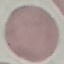

{
  "result": "no malaria parasites detected",
  "preparation": "thin blood smear",
  "capture": "smartphone camera at the microscope eyepiece",
  "image_type": "automatically extracted cell patch, resized to 64 × 64 pixels",
  "stain": "Giemsa"
}